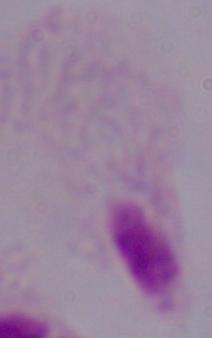

{
  "identification": "trichomonad",
  "magnification": "1000x",
  "modality": "photomicrograph"
}